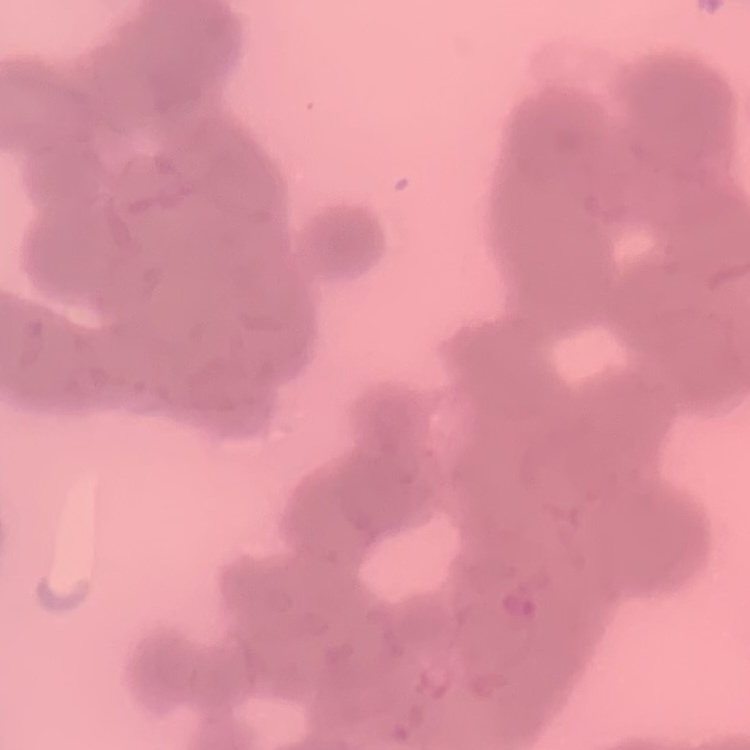
erythrocyte_morphology: rouleaux formation
stain: Field's or Giemsa
image_type: one tile cut from a larger photomicrograph
preparation: thin blood smear